Classify this cell by malaria status.
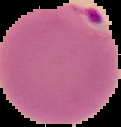
It is parasitized.

preparation = thin blood smear
image type = segmented cell region with the area outside set to black
image size = 121×127 pixels